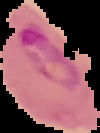

Result: malaria parasites detected. Image is 100×133 pixels. From a thin blood film. Segmented cell region on a black background.